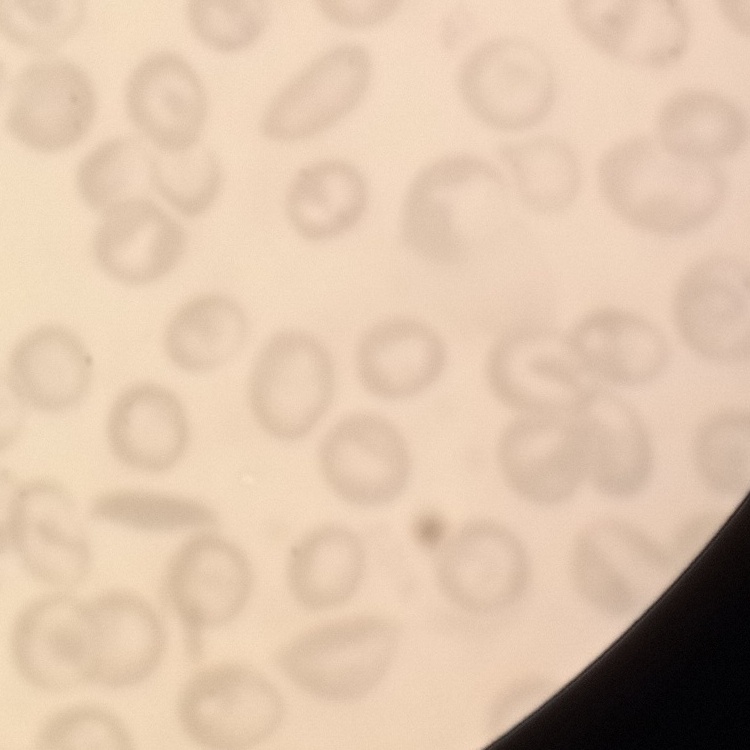
Summary:
  - Red blood cell morphology: no rouleaux formation
  - Preparation: thin blood film
  - Image type: square crop of a larger photomicrograph
  - Stain: Field's or Giemsa